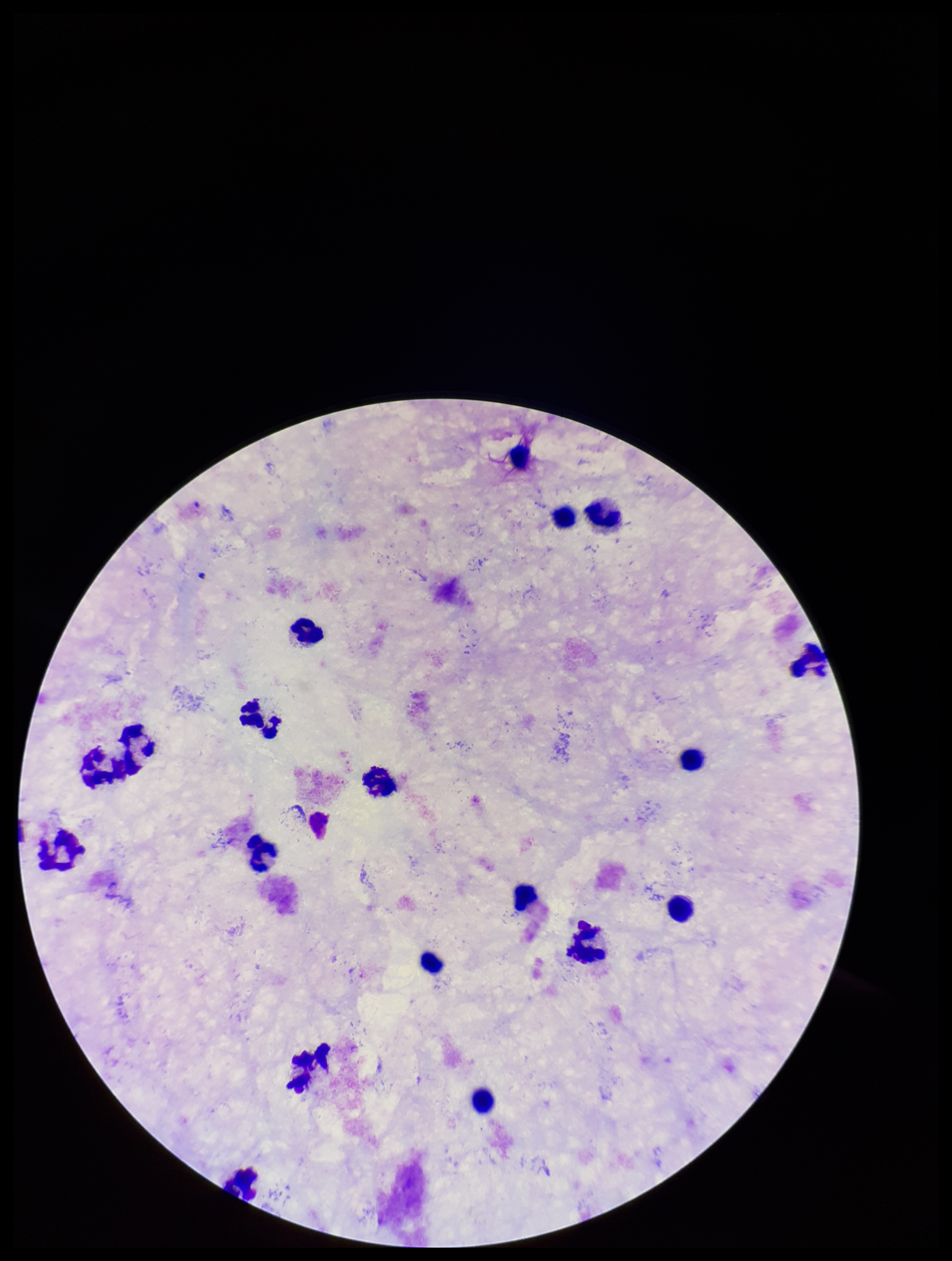
Leukocyte count: 18. Patient malaria status: negative. Giemsa stain. Plasmodium parasites: none identified. Smartphone photograph taken through the eyepiece of a microscope. Image is 952×1261 pixels. Preparation: thick smear. Parasite count: 0. One field from this slide.